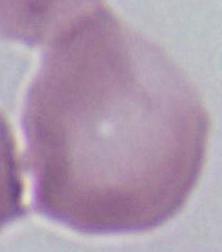
An erythrocyte is shown. Micrograph. Captured at 1000x magnification.